Identify the cell.
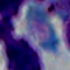

This is a leukocyte.

{
  "modality": "photomicrograph",
  "magnification": "1000x"
}